Point out each Plasmodium parasite.
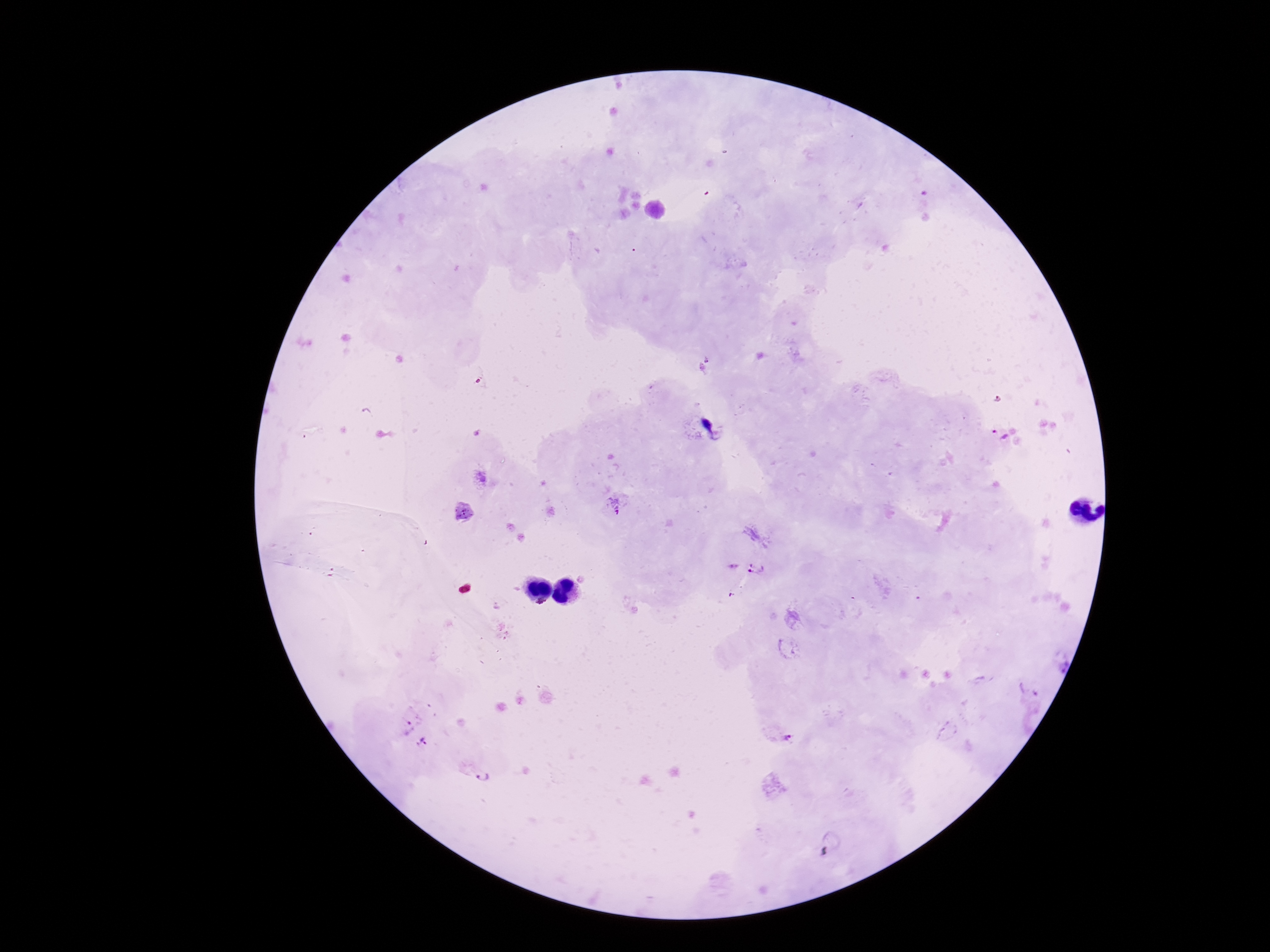
Approximate centers as {x, y} in pixels.
Plasmodium parasites: {715, 426}, {1000, 434}, {616, 506}, {756, 567}, {1031, 688}, {407, 725}, {786, 738}, {426, 745}, {483, 772}.

Summary:
  - Preparation: thick peripheral-blood smear
  - Capture: smartphone camera through the microscope eyepiece
  - Patient malaria status: infected
  - Field of view: single
  - Magnification: 100x
  - Stain: Giemsa
  - Image size: 1270×952 pixels